Report the malaria status of this cell.
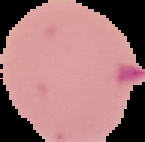

It is parasitized.

Summary:
  - Preparation: thin blood film
  - Image size: 145×142 pixels
  - Image type: cell region segmented out of the field of view; surrounding area masked to black